Assess this cell for malaria.
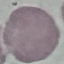

It is uninfected.

image type = cell patch, automatically extracted from a larger field of view and resized to 64 × 64 pixels
capture = smartphone camera at the microscope eyepiece
preparation = thin blood film
stain = Giemsa